Assess this cell for malaria.
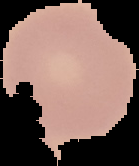
Uninfected.

Summary:
  - Image type: cell region segmented out of the field of view; surrounding area masked to black
  - Image size: 139×166 pixels
  - Preparation: thin blood smear